Identify the blood parasite species.
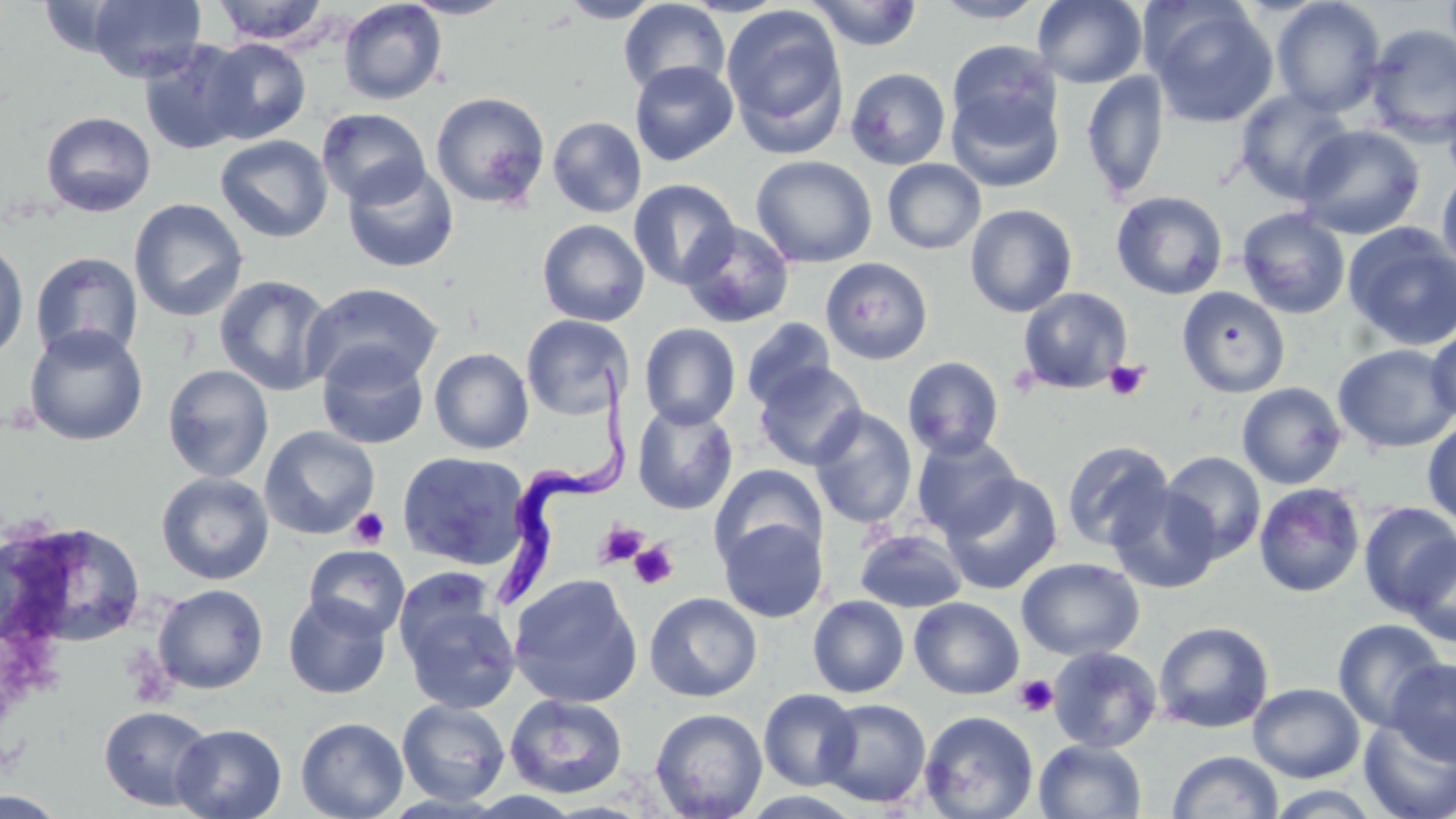

Trypanosoma brucei.

Summary:
  - Coordinate format: approximate bounding boxes as named x1/y1/x2/y2 corners in pixels
  - Uninfected red blood cell locations: (x1=87, y1=0, x2=207, y2=83), (x1=211, y1=0, x2=332, y2=46), (x1=400, y1=0, x2=517, y2=19), (x1=557, y1=0, x2=664, y2=23), (x1=618, y1=0, x2=730, y2=98), (x1=807, y1=0, x2=923, y2=51), (x1=931, y1=0, x2=1048, y2=23), (x1=1033, y1=0, x2=1147, y2=88), (x1=1270, y1=0, x2=1387, y2=117), (x1=338, y1=1, x2=447, y2=105), (x1=1145, y1=2, x2=1279, y2=127), (x1=721, y1=3, x2=849, y2=153), (x1=1364, y1=24, x2=1456, y2=145), (x1=201, y1=37, x2=311, y2=144), (x1=136, y1=39, x2=253, y2=155), (x1=946, y1=39, x2=1061, y2=139), (x1=629, y1=61, x2=738, y2=166), (x1=846, y1=68, x2=950, y2=170), (x1=1081, y1=70, x2=1170, y2=200), (x1=948, y1=87, x2=1064, y2=192), (x1=1235, y1=89, x2=1355, y2=203), (x1=431, y1=92, x2=550, y2=209), (x1=316, y1=108, x2=431, y2=208), (x1=41, y1=111, x2=156, y2=217), (x1=547, y1=116, x2=647, y2=218), (x1=1295, y1=124, x2=1426, y2=240), (x1=215, y1=134, x2=333, y2=243), (x1=750, y1=155, x2=878, y2=268), (x1=882, y1=159, x2=986, y2=254), (x1=342, y1=162, x2=459, y2=273), (x1=1437, y1=168, x2=1456, y2=275), (x1=628, y1=179, x2=740, y2=290), (x1=1111, y1=190, x2=1229, y2=300), (x1=129, y1=198, x2=249, y2=322), (x1=964, y1=204, x2=1078, y2=317), (x1=1236, y1=207, x2=1351, y2=319), (x1=537, y1=219, x2=650, y2=326), (x1=678, y1=220, x2=795, y2=329), (x1=1343, y1=222, x2=1456, y2=351), (x1=0, y1=236, x2=29, y2=362), (x1=29, y1=252, x2=144, y2=362), (x1=820, y1=256, x2=935, y2=366), (x1=213, y1=275, x2=336, y2=396), (x1=302, y1=282, x2=444, y2=392), (x1=1177, y1=286, x2=1291, y2=398), (x1=1018, y1=287, x2=1133, y2=394), (x1=521, y1=314, x2=632, y2=420), (x1=741, y1=318, x2=836, y2=411), (x1=639, y1=323, x2=741, y2=429), (x1=23, y1=324, x2=149, y2=446), (x1=1425, y1=324, x2=1456, y2=424), (x1=316, y1=342, x2=430, y2=450), (x1=1333, y1=343, x2=1456, y2=453), (x1=429, y1=347, x2=534, y2=454), (x1=902, y1=356, x2=1004, y2=460), (x1=753, y1=361, x2=868, y2=471), (x1=162, y1=364, x2=274, y2=483), (x1=1236, y1=382, x2=1348, y2=489), (x1=632, y1=403, x2=739, y2=515), (x1=808, y1=407, x2=917, y2=530), (x1=1422, y1=417, x2=1456, y2=526), (x1=260, y1=425, x2=380, y2=540), (x1=911, y1=434, x2=1023, y2=540), (x1=1060, y1=440, x2=1174, y2=552), (x1=1159, y1=450, x2=1267, y2=563), (x1=397, y1=451, x2=531, y2=571), (x1=709, y1=463, x2=827, y2=571), (x1=155, y1=472, x2=275, y2=585), (x1=940, y1=472, x2=1063, y2=595), (x1=1253, y1=482, x2=1366, y2=598), (x1=1105, y1=484, x2=1225, y2=594), (x1=1357, y1=502, x2=1456, y2=616), (x1=718, y1=518, x2=828, y2=623), (x1=2, y1=520, x2=147, y2=652), (x1=855, y1=529, x2=967, y2=613), (x1=1401, y1=536, x2=1456, y2=648), (x1=303, y1=545, x2=411, y2=640), (x1=1016, y1=557, x2=1144, y2=661), (x1=508, y1=574, x2=644, y2=708), (x1=153, y1=584, x2=269, y2=694), (x1=399, y1=588, x2=521, y2=715), (x1=644, y1=591, x2=763, y2=703), (x1=283, y1=594, x2=392, y2=699), (x1=808, y1=595, x2=909, y2=697), (x1=909, y1=596, x2=1025, y2=700), (x1=1332, y1=618, x2=1447, y2=731), (x1=1152, y1=621, x2=1275, y2=734), (x1=1047, y1=645, x2=1162, y2=753), (x1=1386, y1=658, x2=1456, y2=766), (x1=1247, y1=682, x2=1365, y2=783), (x1=759, y1=689, x2=861, y2=790), (x1=505, y1=693, x2=630, y2=799), (x1=817, y1=697, x2=932, y2=807), (x1=397, y1=699, x2=510, y2=806), (x1=98, y1=705, x2=215, y2=811), (x1=650, y1=707, x2=768, y2=819), (x1=919, y1=710, x2=1039, y2=819), (x1=295, y1=716, x2=408, y2=819), (x1=1358, y1=716, x2=1456, y2=819), (x1=171, y1=723, x2=287, y2=819), (x1=1034, y1=739, x2=1147, y2=819), (x1=1167, y1=750, x2=1283, y2=818), (x1=1262, y1=785, x2=1387, y2=818)
  - Trypanosoma brucei locations: (x1=492, y1=364, x2=634, y2=607)
  - Platelet locations: (x1=1104, y1=360, x2=1149, y2=401), (x1=348, y1=507, x2=389, y2=549), (x1=595, y1=521, x2=648, y2=568), (x1=629, y1=541, x2=678, y2=589), (x1=1014, y1=675, x2=1059, y2=717)
  - Preparation: thin blood film
  - Image size: 1456×819 pixels
  - Stain: May-Grünwald-Giemsa
  - Modality: optical microscopy
  - Magnification: 1000x
  - Field of view: single